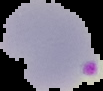 From a thin blood smear. Result: Plasmodium parasites identified. Image is 103×91 pixels. The area outside the segmented cell region is set to black.